Classify this cell by malaria status.
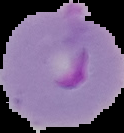
It is parasitized.

Summary:
  - Preparation: thin blood smear
  - Image type: segmented cell region on a black background
  - Image size: 124×133 pixels